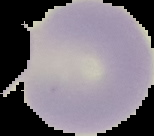

Segmented cell region on a black background. Image is 154×136 pixels. Result: no Plasmodium parasites seen. From a thin blood film.